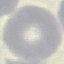 Malaria status: uninfected. Thin blood film. Giemsa stain. Photographed with a smartphone camera at the microscope eyepiece. Automatically extracted cell patch, resized to 64 × 64 pixels.